Assess this cell for malaria.
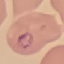

Parasitized.

capture: smartphone camera at the microscope eyepiece
preparation: thin smear
stain: Giemsa
image_type: cell patch, automatically extracted from a larger field of view and resized to 64 × 64 pixels